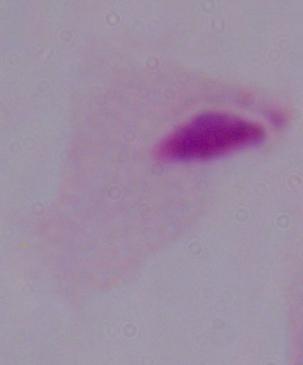 A trichomonad is shown. Photomicrograph. 1000x magnification.